Assess the morphology of the erythrocytes.
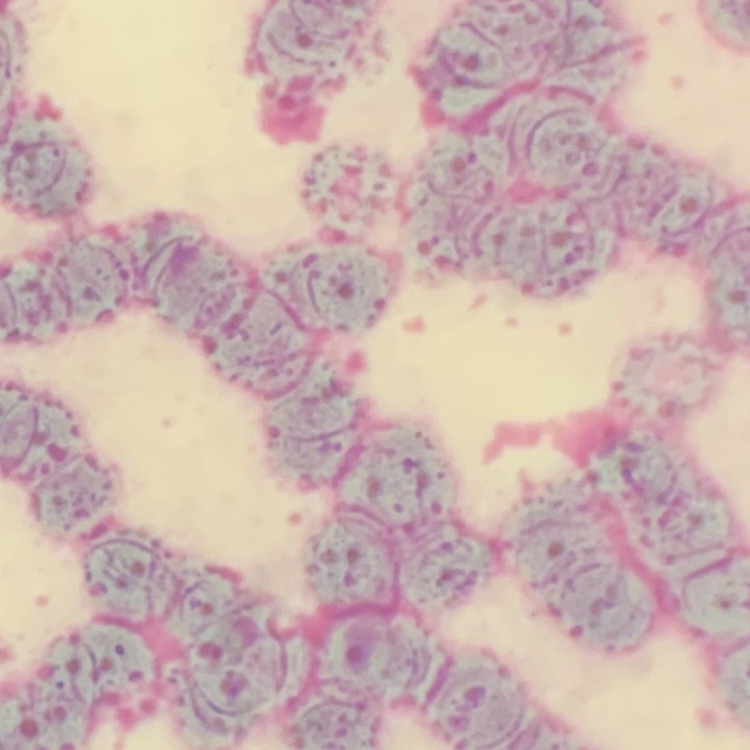

Rouleaux formation.

preparation = thin blood film
stain = Field's or Giemsa
image type = square crop of a larger photomicrograph